Assess this cell for malaria.
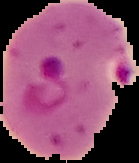

It is parasitized.

image_size: 139×163 pixels
preparation: thin blood film
image_type: segmented cell region on a black background